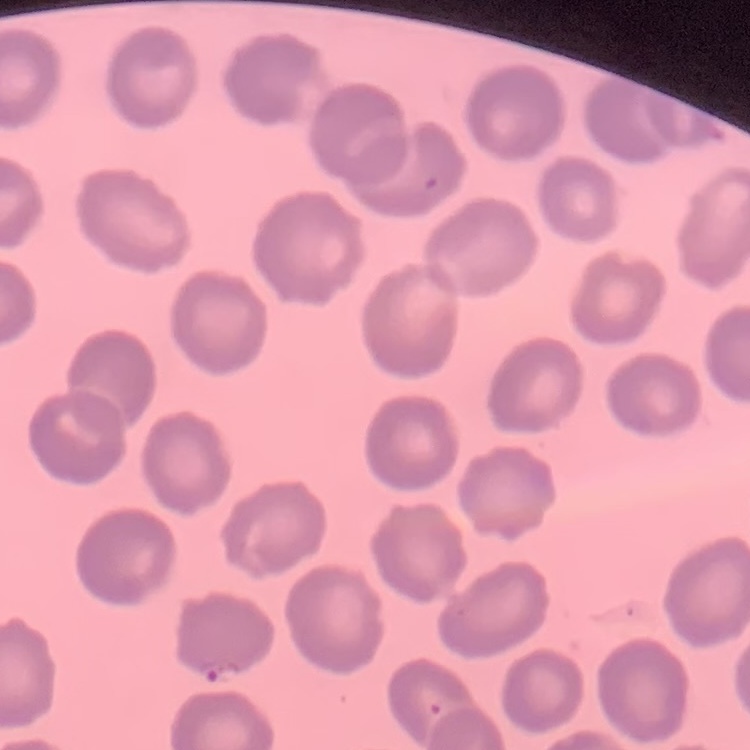

Summary:
  - Red blood cell morphology: no rouleaux formation
  - Stain: Field's or Giemsa
  - Image type: one tile cut from a larger photomicrograph
  - Preparation: thin blood film